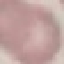
Result: no malaria parasites detected. Thin blood film. Acquired by smartphone through the microscope eyepiece. Cell patch, automatically extracted from a larger field of view and resized to 64 × 64 pixels. Giemsa-stained preparation.